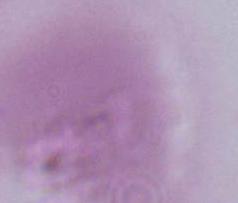
magnification: 1000x
identification: red blood cell
modality: photomicrograph